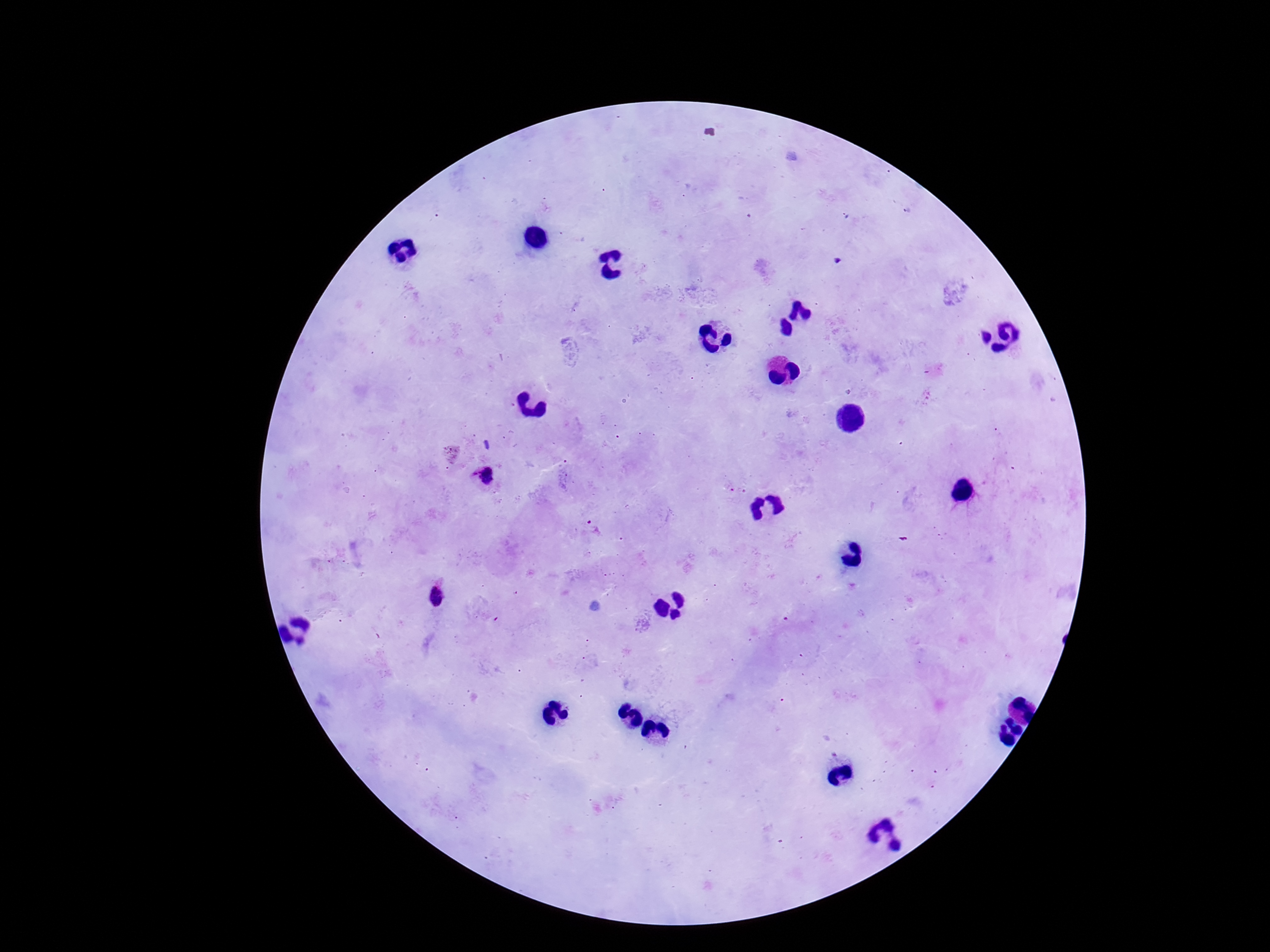 Approximate centers as {x, y} in pixels. Plasmodium parasite locations: {484, 478}, {592, 527}, {439, 595}. 100x magnification. Thick blood film. Image is 1270×952 pixels. Smartphone photograph taken through the microscope eyepiece. Giemsa-stained preparation. Single field of view. Patient malaria status: infected.